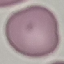
result = negative for malaria parasites
preparation = thin smear
image type = automatically extracted cell patch, resized to 64 × 64 pixels
capture = smartphone camera at the microscope eyepiece
stain = Giemsa